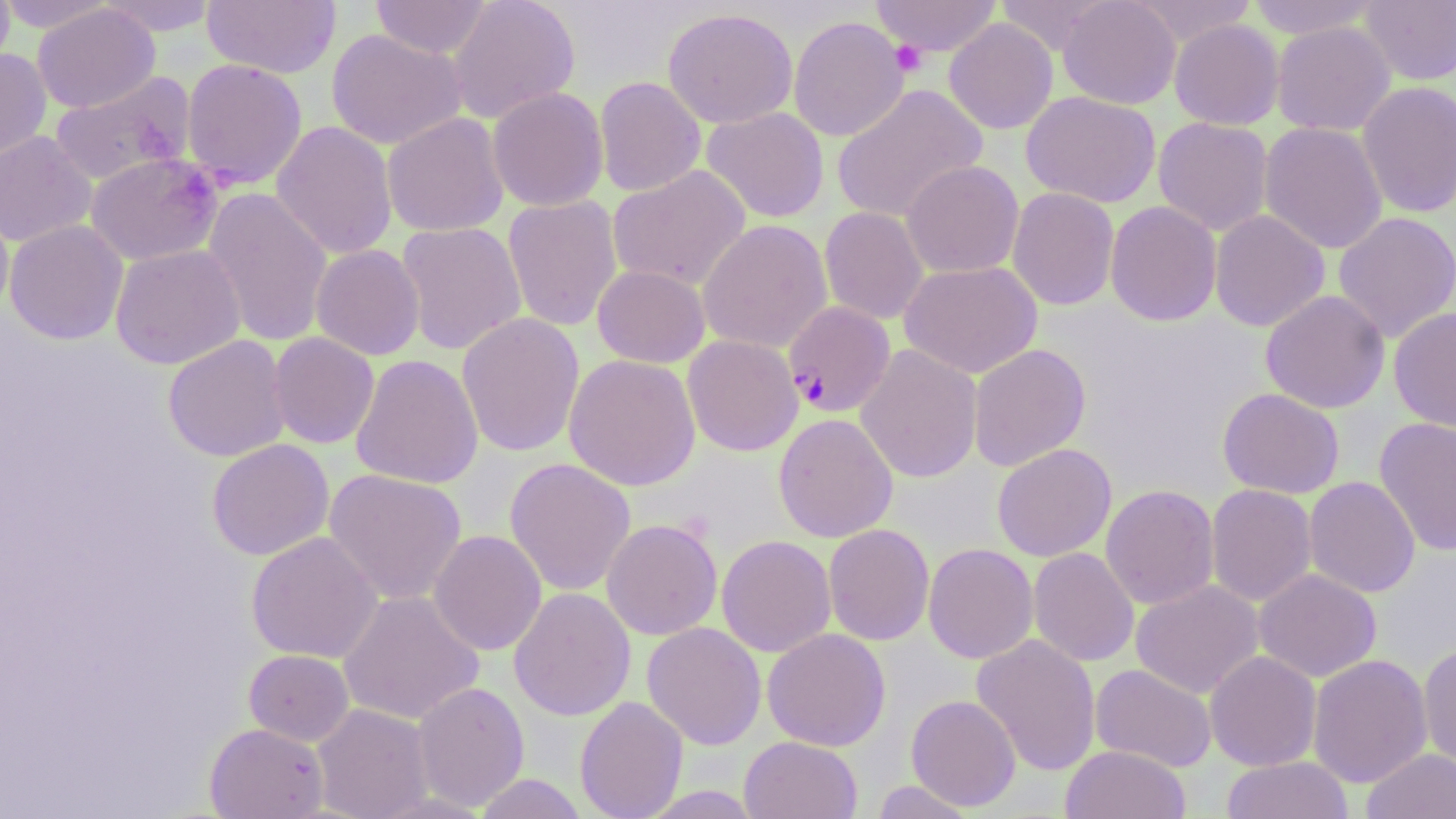

slide-level diagnosis = Plasmodium falciparum
uninfected red blood cell locations = approximate bounding boxes as [x1, y1, x2, y2] in pixels: [0, 0, 15, 76], [0, 0, 115, 33], [96, 0, 221, 36], [201, 0, 341, 78], [371, 0, 492, 59], [447, 0, 581, 123], [870, 0, 1002, 56], [994, 0, 1111, 56], [1058, 0, 1181, 109], [1130, 0, 1261, 47], [1244, 0, 1383, 39], [1359, 0, 1456, 86], [32, 3, 160, 113], [662, 7, 798, 129], [788, 15, 909, 142], [943, 18, 1058, 134], [1169, 19, 1285, 130], [1271, 21, 1396, 137], [326, 28, 469, 150], [0, 47, 51, 162], [181, 58, 308, 189], [49, 71, 196, 186], [595, 76, 706, 197], [1356, 80, 1456, 219], [831, 83, 988, 224], [487, 87, 609, 211], [1021, 91, 1161, 208], [701, 107, 829, 223], [382, 112, 509, 237], [1153, 117, 1273, 236], [271, 121, 398, 260], [1259, 121, 1388, 254], [0, 131, 98, 247], [86, 152, 224, 266], [901, 160, 1024, 278], [607, 165, 751, 292], [202, 187, 334, 347], [1007, 187, 1120, 310], [502, 195, 622, 332], [1105, 200, 1222, 326], [0, 202, 14, 319], [819, 206, 929, 325], [1209, 210, 1330, 332], [1333, 211, 1456, 344], [4, 219, 128, 345], [698, 220, 832, 353], [396, 221, 527, 355], [110, 244, 245, 369], [310, 244, 425, 360], [899, 261, 1042, 378], [592, 265, 710, 367], [1260, 290, 1391, 414], [1388, 307, 1456, 433], [457, 312, 585, 457], [268, 332, 380, 449], [163, 335, 291, 462], [682, 335, 803, 456], [968, 343, 1091, 471], [856, 344, 983, 483], [350, 354, 484, 489], [563, 354, 701, 491], [1217, 387, 1345, 499], [773, 413, 898, 543], [1373, 417, 1456, 557], [207, 439, 334, 560], [992, 443, 1116, 562], [504, 457, 636, 596], [324, 468, 467, 605], [1304, 476, 1420, 598], [1100, 484, 1219, 609], [1206, 484, 1318, 607], [601, 519, 723, 640], [823, 524, 935, 645], [428, 530, 547, 655], [246, 531, 383, 663], [717, 535, 836, 657], [923, 543, 1038, 663], [1028, 547, 1140, 667], [1253, 568, 1382, 682], [1131, 580, 1264, 698], [509, 587, 636, 720], [338, 590, 484, 725], [642, 622, 766, 750], [762, 628, 891, 751], [971, 634, 1101, 776], [1418, 641, 1456, 771], [244, 649, 354, 745], [1205, 650, 1322, 771], [1307, 654, 1433, 789], [1090, 664, 1217, 772], [412, 682, 529, 811], [906, 694, 1021, 811], [574, 696, 688, 819], [313, 704, 433, 819], [205, 722, 329, 818], [739, 736, 862, 819], [1060, 744, 1190, 819], [1361, 748, 1456, 819], [1221, 756, 1355, 819], [475, 773, 588, 818], [870, 780, 978, 818], [639, 785, 764, 818]
stain = May-Grünwald-Giemsa
modality = light microscopy
Plasmodium falciparum-infected red blood cell locations = approximate bounding boxes as [x1, y1, x2, y2] in pixels: [783, 301, 896, 418]
preparation = thin blood smear
field of view = single
magnification = 1000x
platelet locations = approximate bounding boxes as [x1, y1, x2, y2] in pixels: [890, 41, 927, 77]
image size = 1456×819 pixels